Point out each malaria parasite.
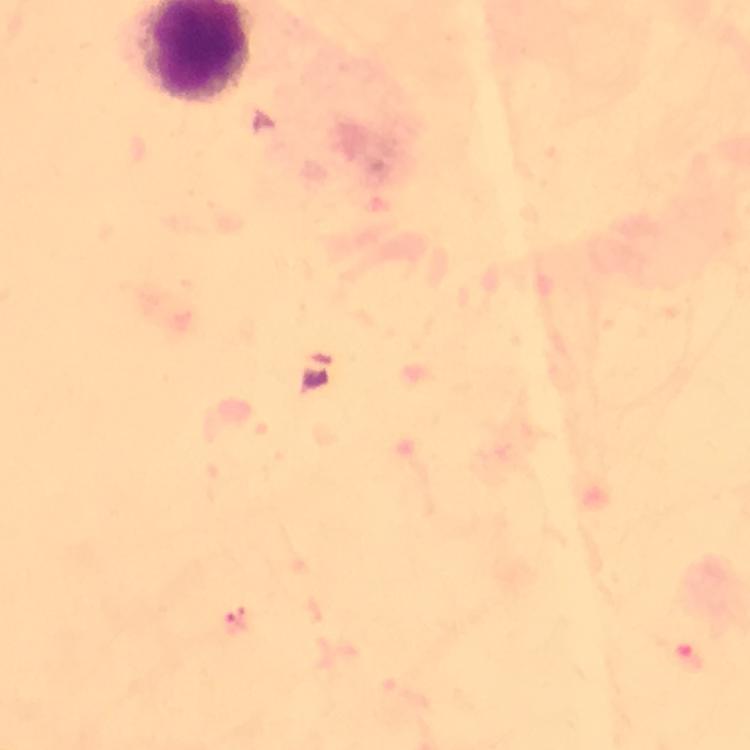
Approximate centers as {x, y} in pixels.
Malaria parasites: {236, 624}.

Summary:
  - Cropped from: a single field of view
  - Stain: Giemsa
  - Preparation: thick blood film
  - Magnification: 100x
  - Image size: 750×750 pixels
  - Immersion oil: used
  - Capture: smartphone camera through the microscope
  - Context: from a malaria diagnostic workup